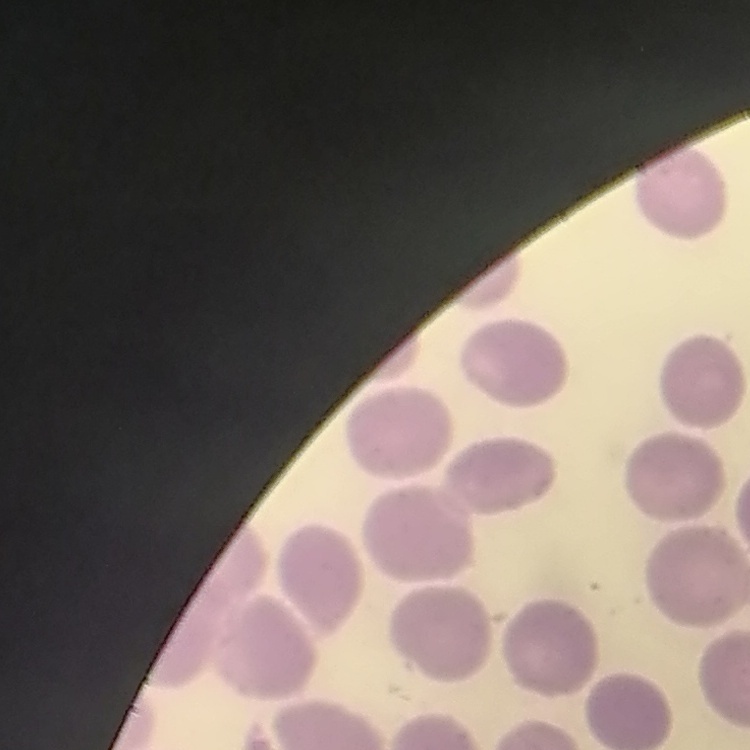

erythrocyte morphology = no rouleaux formation
image type = square crop of a larger photomicrograph
preparation = thin blood film
stain = Field's or Giemsa